Report the malaria status of this cell.
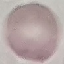

It is uninfected.

Acquired by smartphone through the microscope eyepiece. Giemsa-stained preparation. Cell patch, automatically extracted from a larger field of view and resized to 64 × 64 pixels. Thin blood smear.